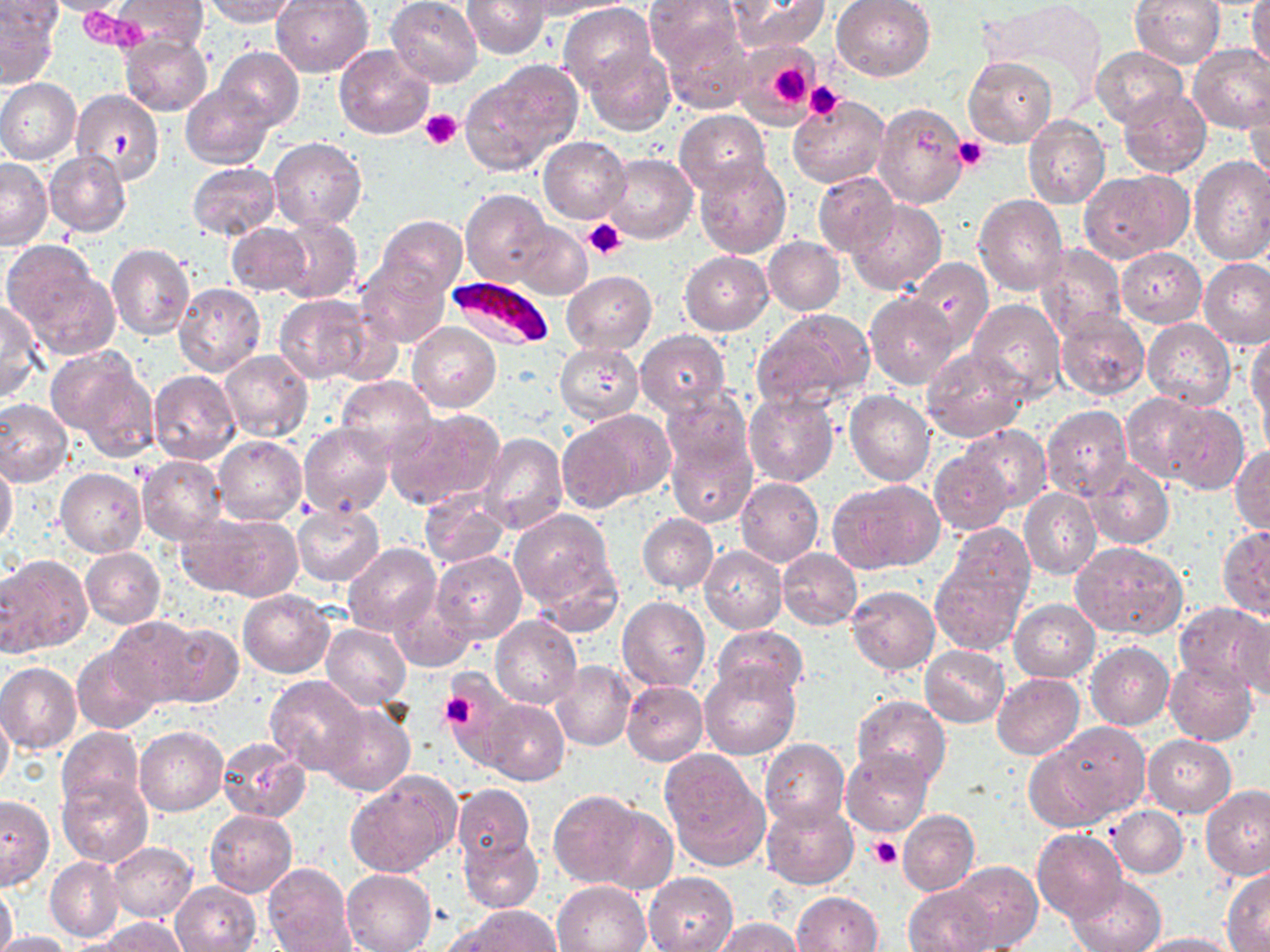 Approximate bounding boxes as [x1, y1, x2, y2] in pixels. Plasmodium falciparum-infected red blood cell locations: [444, 274, 556, 353]. Uninfected red blood cell locations: [35, 0, 136, 16], [114, 0, 206, 52], [204, 0, 299, 26], [270, 0, 374, 76], [386, 0, 483, 88], [462, 0, 550, 59], [529, 0, 630, 17], [646, 0, 746, 76], [728, 0, 830, 53], [830, 0, 936, 81], [1130, 0, 1224, 68], [1249, 0, 1270, 74], [976, 1, 1110, 99], [559, 3, 655, 97], [1, 4, 61, 85], [658, 18, 754, 113], [120, 34, 212, 114], [737, 42, 819, 115], [334, 43, 435, 139], [1189, 43, 1270, 132], [1091, 46, 1188, 128], [216, 47, 303, 128], [584, 49, 675, 132], [964, 56, 1056, 149], [462, 63, 581, 176], [894, 67, 1040, 161], [0, 78, 81, 165], [180, 83, 276, 169], [70, 88, 163, 184], [1119, 88, 1212, 176], [1244, 92, 1270, 187], [788, 96, 890, 188], [875, 99, 969, 209], [674, 109, 771, 195], [1023, 115, 1110, 208], [539, 136, 629, 223], [268, 138, 366, 231], [44, 151, 132, 236], [605, 152, 698, 243], [695, 156, 792, 259], [1188, 157, 1270, 266], [0, 158, 52, 249], [187, 162, 280, 241], [1078, 170, 1192, 263], [813, 172, 899, 258], [461, 189, 551, 285], [973, 193, 1068, 297], [847, 200, 945, 294], [275, 214, 362, 304], [375, 214, 467, 299], [510, 222, 592, 298], [226, 223, 311, 297], [763, 237, 845, 315], [2, 242, 113, 353], [106, 243, 195, 340], [1037, 244, 1126, 341], [1118, 247, 1205, 326], [679, 250, 773, 335], [355, 257, 448, 347], [907, 259, 993, 351], [1200, 259, 1270, 349], [562, 270, 656, 353], [173, 283, 265, 377], [865, 292, 961, 388], [273, 294, 374, 384], [968, 298, 1066, 403], [0, 299, 43, 403], [753, 308, 875, 413], [1053, 308, 1150, 401], [1142, 319, 1236, 408], [407, 324, 501, 412], [635, 330, 731, 419], [1248, 333, 1270, 424], [554, 342, 644, 423], [921, 347, 1028, 441], [48, 348, 159, 459], [219, 350, 312, 440], [148, 370, 241, 465], [337, 375, 437, 460], [1258, 375, 1270, 461], [661, 387, 752, 476], [845, 391, 936, 486], [743, 392, 839, 488], [1119, 392, 1217, 482], [0, 398, 73, 488], [1162, 403, 1249, 495], [1041, 405, 1133, 500], [385, 407, 505, 510], [558, 410, 670, 510], [297, 422, 394, 519], [410, 422, 557, 523], [958, 423, 1051, 511], [479, 434, 568, 534], [213, 436, 306, 524], [665, 438, 756, 528], [1231, 446, 1270, 534], [928, 447, 1014, 534], [138, 455, 228, 543], [1085, 459, 1173, 550], [0, 460, 17, 549], [56, 468, 147, 558], [735, 478, 823, 565], [829, 478, 944, 574], [418, 487, 512, 570], [1019, 487, 1100, 579], [291, 504, 384, 586], [510, 508, 618, 611], [178, 513, 298, 599], [638, 513, 718, 594], [942, 524, 1035, 616], [1217, 527, 1270, 619], [1072, 541, 1188, 640], [343, 543, 440, 636], [699, 546, 786, 634], [81, 547, 165, 629], [777, 548, 862, 630], [930, 550, 1030, 659], [431, 551, 527, 644], [1, 556, 91, 656], [846, 585, 940, 674], [237, 591, 334, 677], [388, 591, 476, 670], [617, 597, 710, 693], [1009, 599, 1100, 682], [1174, 602, 1270, 693], [1232, 611, 1269, 700], [489, 614, 581, 709], [106, 616, 206, 707], [161, 622, 241, 706], [320, 622, 411, 710], [711, 625, 808, 705], [72, 641, 163, 733], [1086, 641, 1174, 731], [920, 645, 1009, 726], [1164, 659, 1258, 745], [550, 661, 635, 751], [0, 662, 82, 754], [698, 664, 800, 759], [437, 670, 521, 763], [993, 673, 1084, 760], [264, 675, 367, 776], [620, 681, 707, 766], [851, 695, 950, 790], [481, 699, 569, 785], [320, 702, 414, 797], [0, 703, 13, 793], [1049, 723, 1148, 823], [134, 726, 227, 815], [58, 727, 144, 813], [1143, 735, 1236, 817], [217, 737, 311, 823], [760, 739, 849, 831], [1025, 743, 1118, 831], [841, 748, 933, 836], [661, 753, 769, 870], [346, 773, 458, 877], [57, 776, 151, 868], [452, 784, 534, 865], [1200, 784, 1269, 880], [549, 789, 646, 888], [0, 796, 55, 889], [761, 800, 858, 889], [586, 802, 679, 895], [1108, 805, 1188, 878], [204, 810, 297, 897], [898, 810, 979, 895], [1032, 828, 1127, 922], [458, 831, 545, 913], [108, 841, 198, 923], [45, 857, 123, 941], [950, 860, 1042, 950], [263, 863, 355, 952], [342, 868, 435, 952], [1224, 870, 1270, 950], [644, 871, 738, 952], [1066, 873, 1166, 952], [551, 880, 651, 952], [169, 881, 262, 951], [0, 883, 18, 952], [902, 883, 999, 952], [791, 890, 884, 952], [452, 906, 562, 952], [97, 917, 188, 952], [713, 918, 806, 952], [0, 930, 74, 952], [1135, 932, 1238, 952]. Platelet locations: [80, 8, 143, 49], [765, 63, 812, 109], [803, 82, 844, 122], [420, 109, 463, 151], [107, 131, 136, 160], [953, 136, 989, 172], [582, 217, 627, 259], [437, 690, 476, 730], [869, 836, 903, 870]. Slide-level diagnosis: Plasmodium falciparum. Thin blood film. One field of a larger specimen. Light microscopy. May-Grünwald-Giemsa stain. Image is 1270×952 pixels. Captured at 1000x magnification.